Locate and identify every blood parasite.
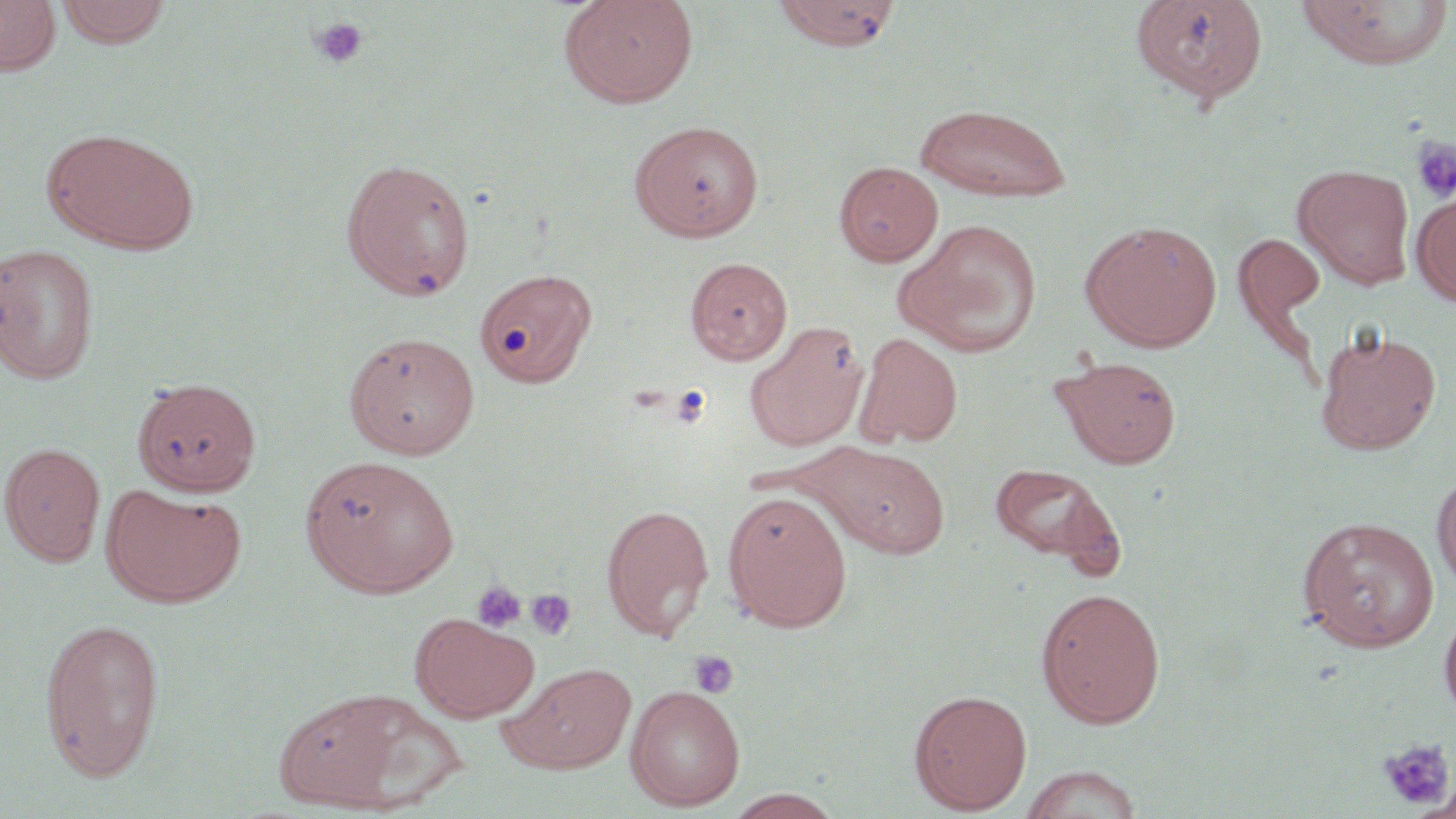
No blood parasites observed.

{
  "slide_level_diagnosis": "negative for blood parasites",
  "uninfected_red_blood_cell_locations": "approximate bounding boxes as named x1/y1/x2/y2 corners in pixels: (x1=0, y1=0, x2=62, y2=76), (x1=55, y1=0, x2=173, y2=48), (x1=559, y1=0, x2=699, y2=108), (x1=772, y1=0, x2=901, y2=51), (x1=1130, y1=0, x2=1269, y2=105), (x1=1294, y1=0, x2=1454, y2=69), (x1=914, y1=102, x2=1073, y2=202), (x1=629, y1=120, x2=764, y2=241), (x1=50, y1=130, x2=199, y2=254), (x1=340, y1=157, x2=476, y2=301), (x1=834, y1=161, x2=943, y2=266), (x1=1293, y1=163, x2=1415, y2=289), (x1=1412, y1=189, x2=1456, y2=306), (x1=899, y1=219, x2=1044, y2=357), (x1=1080, y1=220, x2=1222, y2=351), (x1=1233, y1=231, x2=1328, y2=340), (x1=0, y1=242, x2=101, y2=384), (x1=685, y1=257, x2=793, y2=365), (x1=474, y1=267, x2=598, y2=387), (x1=745, y1=322, x2=868, y2=452), (x1=1315, y1=328, x2=1440, y2=455), (x1=344, y1=330, x2=481, y2=460), (x1=853, y1=331, x2=963, y2=449), (x1=1053, y1=355, x2=1181, y2=468), (x1=0, y1=442, x2=105, y2=566), (x1=812, y1=442, x2=951, y2=559), (x1=300, y1=455, x2=459, y2=597), (x1=988, y1=462, x2=1124, y2=571), (x1=1432, y1=467, x2=1456, y2=593), (x1=101, y1=484, x2=246, y2=608), (x1=722, y1=490, x2=852, y2=631), (x1=601, y1=502, x2=714, y2=642), (x1=1297, y1=515, x2=1439, y2=652), (x1=1036, y1=587, x2=1166, y2=728), (x1=1438, y1=602, x2=1456, y2=726), (x1=411, y1=614, x2=540, y2=721), (x1=39, y1=616, x2=166, y2=781), (x1=500, y1=662, x2=636, y2=773), (x1=625, y1=684, x2=745, y2=811), (x1=272, y1=687, x2=445, y2=813), (x1=909, y1=688, x2=1032, y2=813), (x1=1018, y1=764, x2=1145, y2=819), (x1=722, y1=789, x2=846, y2=819)",
  "modality": "light microscopy",
  "preparation": "thin blood smear",
  "magnification": "1000x",
  "image_size": "1456×819 pixels",
  "stain": "May-Grünwald-Giemsa",
  "platelet_locations": "approximate bounding boxes as named x1/y1/x2/y2 corners in pixels: (x1=310, y1=16, x2=368, y2=68), (x1=1411, y1=138, x2=1456, y2=202), (x1=669, y1=384, x2=713, y2=428), (x1=471, y1=581, x2=528, y2=633), (x1=526, y1=588, x2=578, y2=640), (x1=688, y1=650, x2=739, y2=698), (x1=1377, y1=738, x2=1454, y2=810)",
  "field_of_view": "single"
}